Describe the morphology of the erythrocytes.
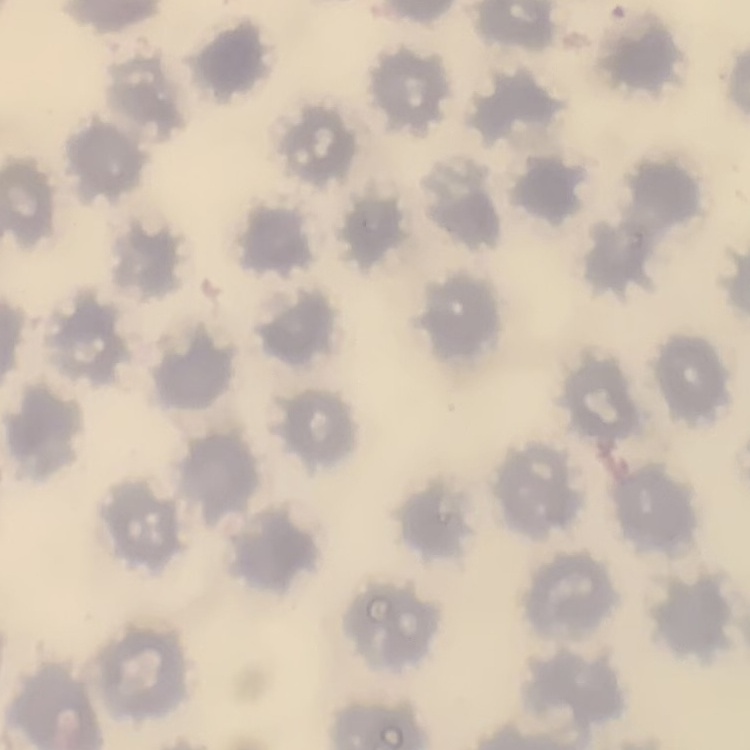
They show no rouleaux formation.

Summary:
  - Image type: square crop of a larger photomicrograph
  - Stain: Field's or Giemsa
  - Preparation: thin blood smear